Comment on the morphology of the red blood cells.
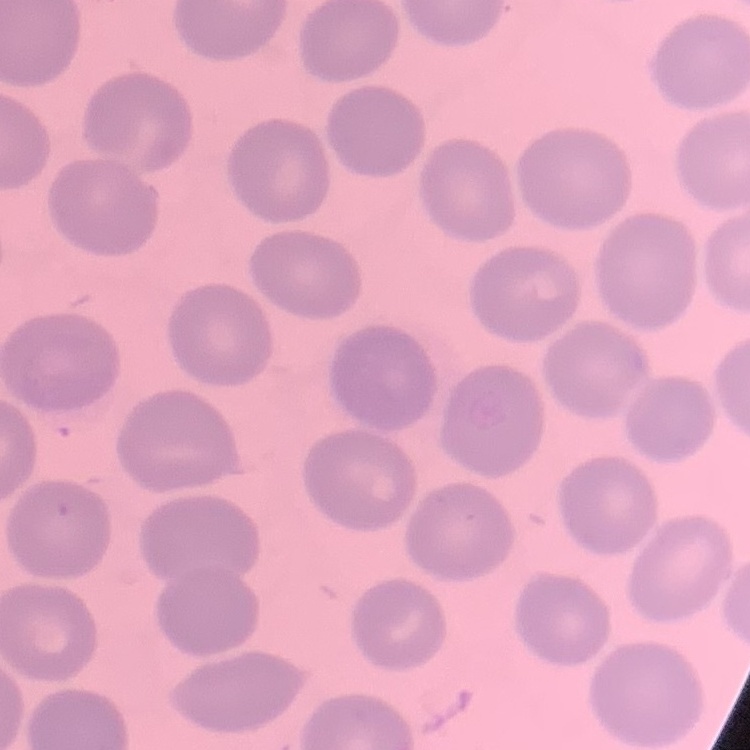
No rouleaux formation.

Summary:
  - Preparation: thin blood smear
  - Image type: one tile cut from a larger photomicrograph
  - Stain: Field's or Giemsa